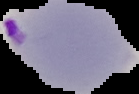

Summary:
  - Image type: segmented cell region with the area outside set to black
  - Malaria status: parasitized
  - Preparation: thin blood smear
  - Image size: 139×94 pixels